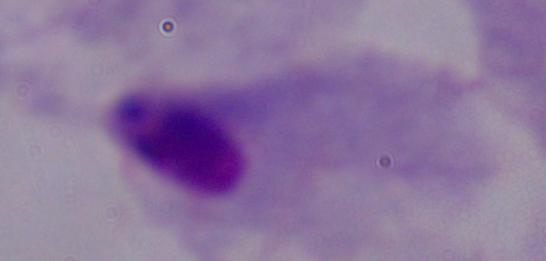

modality: micrograph
identification: trichomonad
magnification: 1000x